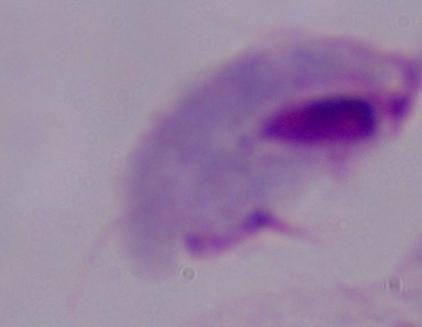

magnification: 1000x
modality: micrograph
identification: trichomonad